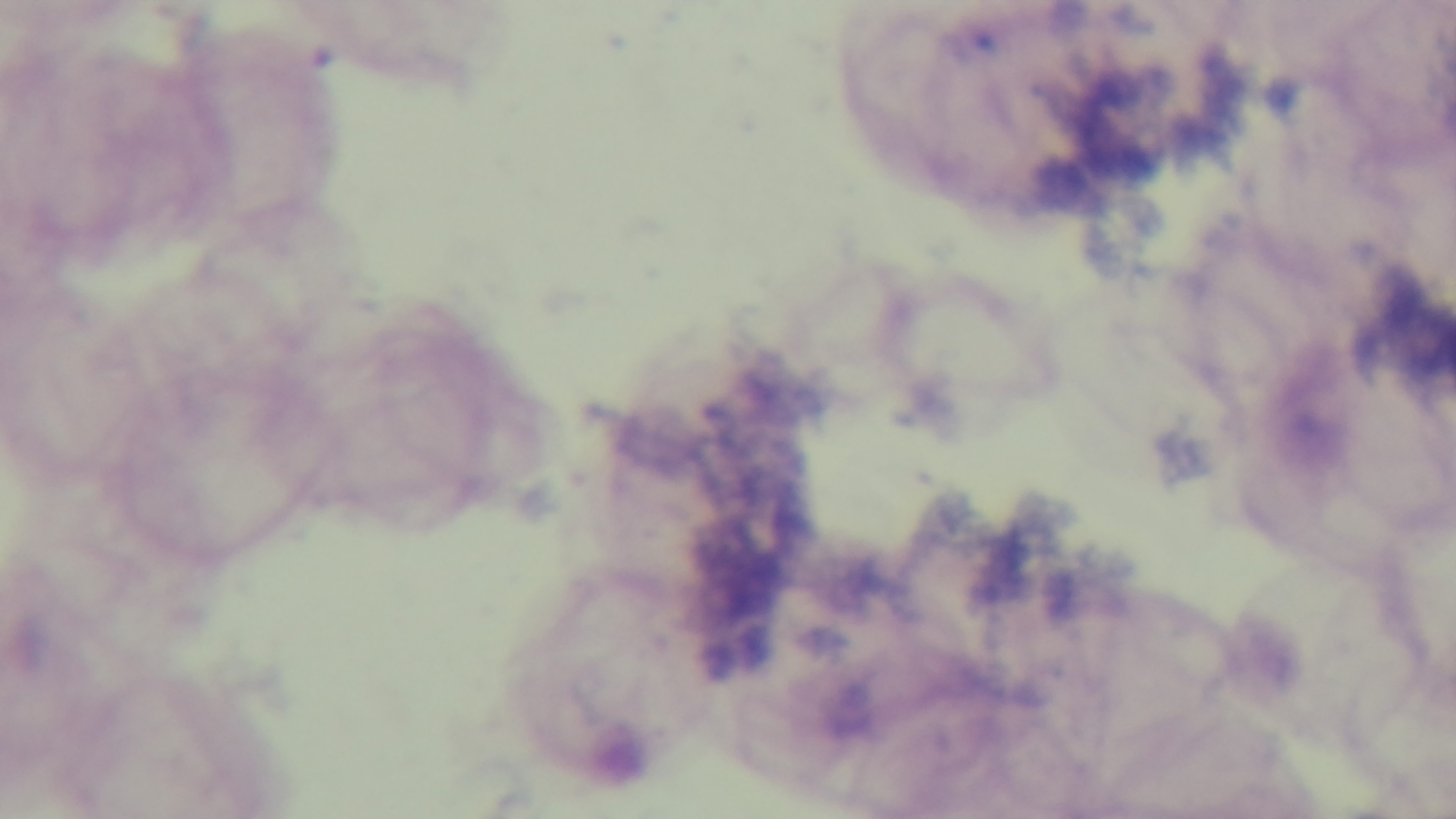

malaria status = negative
capture = mounted 4K digital camera
modality = light microscopy
field of view = one from the slide
stain = Giemsa
preparation = thick blood film
objective = 100x oil immersion